Comment on the morphology of the red blood cells.
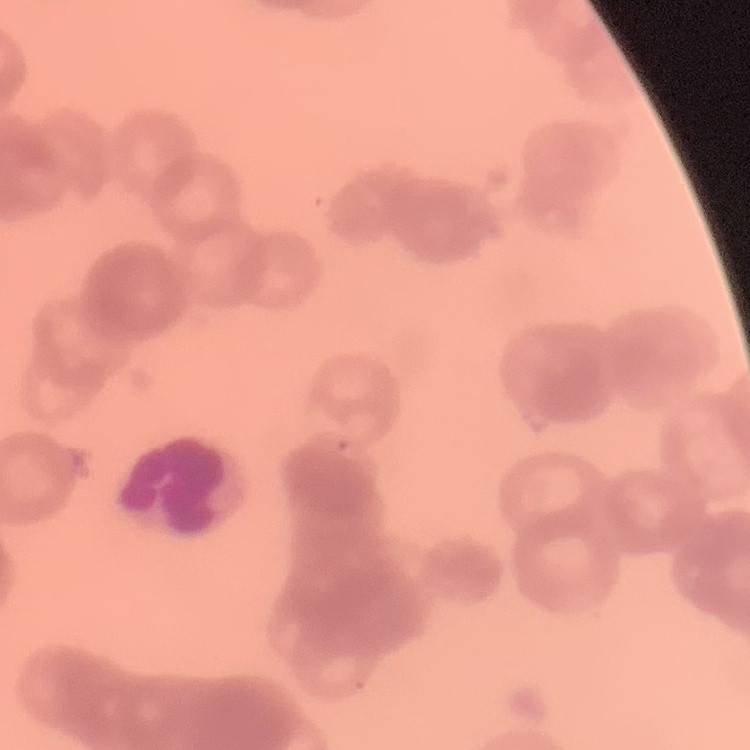
They show rouleaux formation.

preparation: thin blood smear
stain: Field's or Giemsa
image_type: one tile cut from a larger photomicrograph